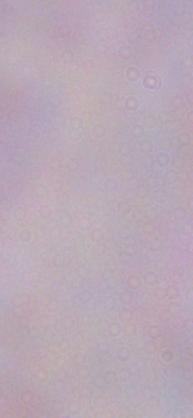

Micrograph. 1000x magnification. A trypanosome is seen.